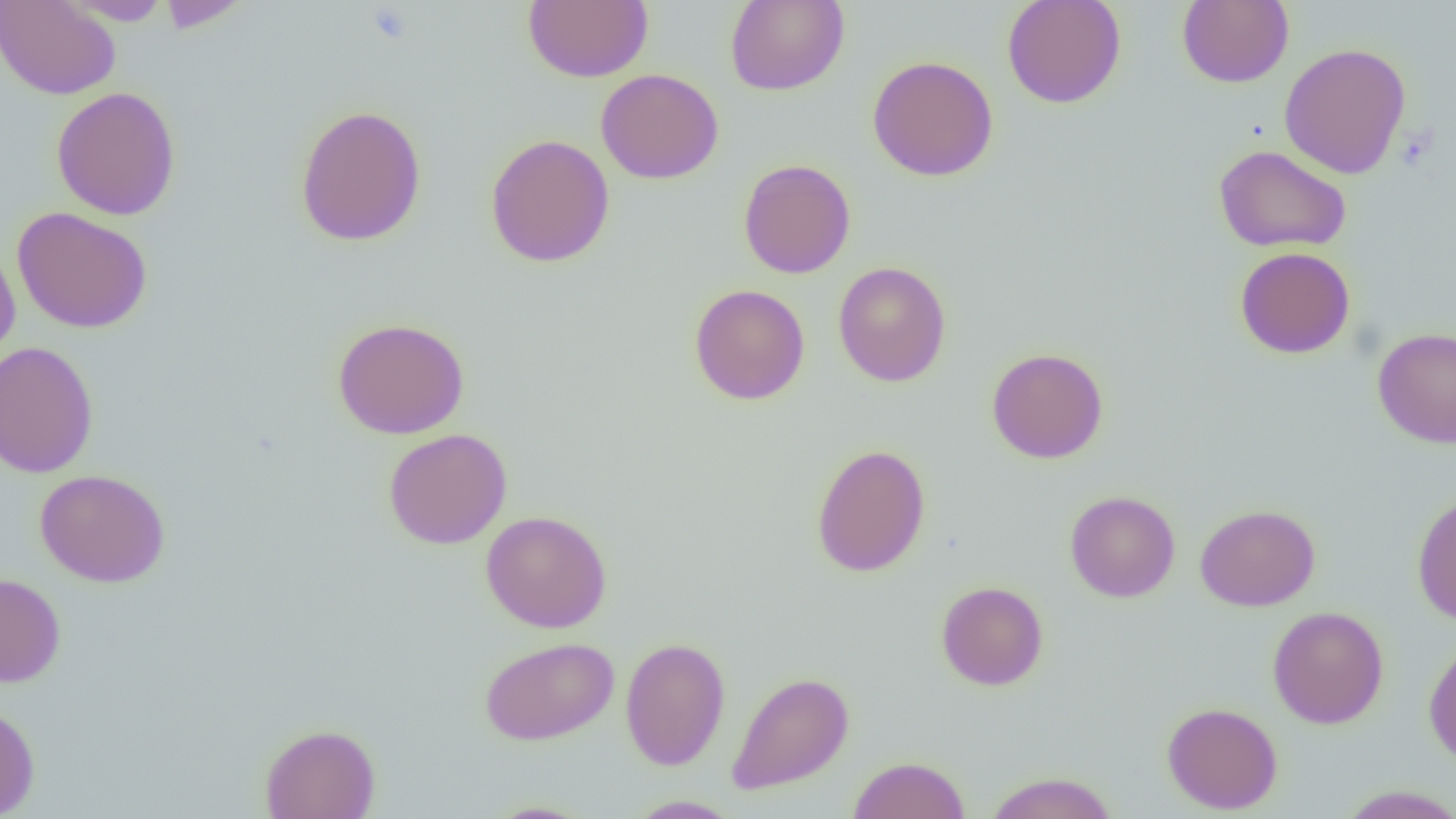

Summary:
  - Coordinate format: approximate bounding boxes as (x1,y1)-(x2,y2) corner pairs in pixels
  - Platelet locations: (367,5)-(416,45)
  - Uninfected red blood cell locations: (0,0)-(120,100), (59,0)-(173,25), (157,0)-(249,33), (523,0)-(652,83), (724,0)-(849,96), (1001,0)-(1126,109), (1177,0)-(1294,88), (1279,42)-(1412,179), (867,55)-(998,181), (595,68)-(724,185), (51,86)-(182,221), (294,104)-(428,247), (485,134)-(615,268), (1213,144)-(1351,253), (738,159)-(856,279), (11,207)-(152,333), (0,241)-(20,365), (1234,247)-(1355,359), (832,261)-(951,386), (688,284)-(810,405), (332,317)-(469,439), (1372,327)-(1455,449), (0,340)-(99,478), (986,347)-(1108,464), (383,428)-(512,550), (811,442)-(930,578), (34,468)-(171,587), (1065,490)-(1181,602), (1411,492)-(1456,625), (1195,504)-(1320,611), (481,510)-(612,633), (0,572)-(66,687), (936,581)-(1048,691), (1267,605)-(1389,728), (480,636)-(619,745), (620,636)-(730,771), (1423,636)-(1456,768), (727,671)-(854,795), (1161,702)-(1283,814), (0,704)-(40,818), (259,723)-(380,819), (848,755)-(971,819), (984,771)-(1120,819), (1336,785)-(1456,819), (625,795)-(740,818), (482,800)-(597,818)
  - Slide-level diagnosis: negative for blood parasites
  - Modality: light microscopy
  - Image size: 1456×819 pixels
  - Magnification: 1000x
  - Preparation: thin blood film
  - Field of view: one of a larger specimen